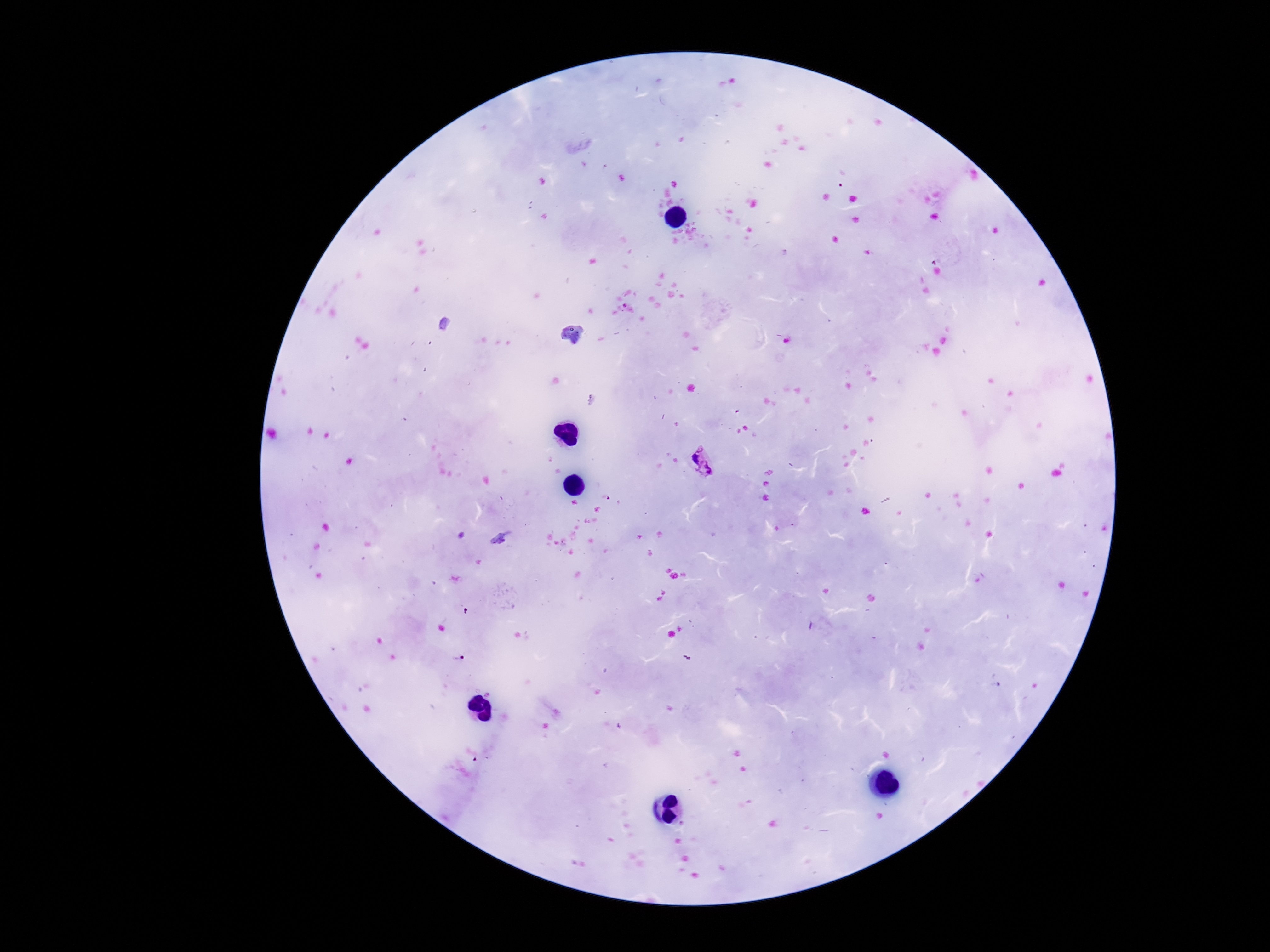

stain: Giemsa
field_of_view: single
capture: smartphone camera through the microscope eyepiece
plasmodium_parasite_locations: 'approximate centers as (x, y) in pixels: (592, 401), (704, 462), (500, 538), (457, 659)'
patient_malaria_status: positive
image_size: 1270×952 pixels
magnification: 100x
preparation: thick peripheral-blood smear